Describe the morphology of the erythrocytes.
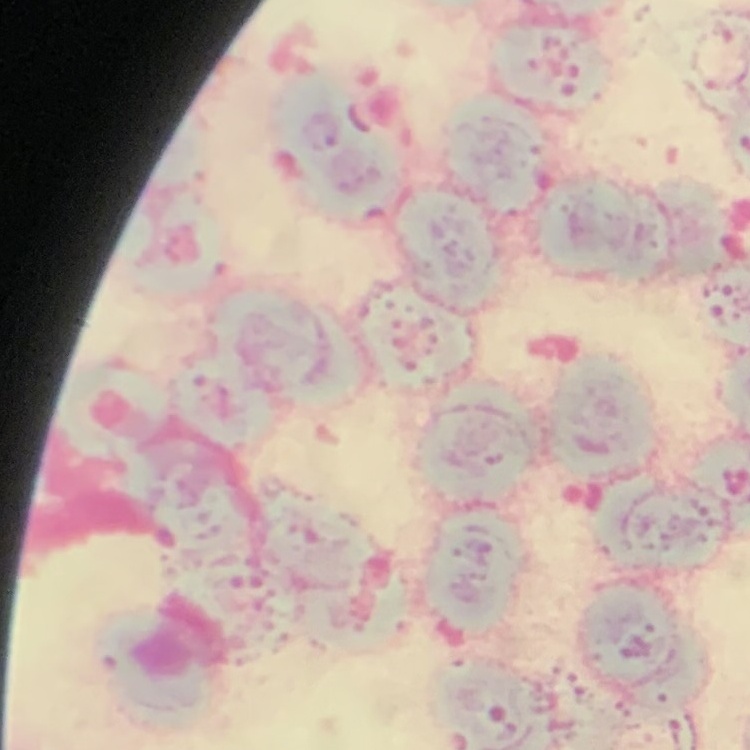
Rouleaux formation.

Summary:
  - Stain: Field's or Giemsa
  - Preparation: thin peripheral smear
  - Image type: one tile cut from a larger photomicrograph